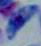
identification: Toxoplasma gondii
magnification: 1000x
modality: micrograph